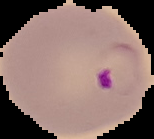

image size = 154×139 pixels
preparation = thin blood film
malaria status = parasitized
image type = segmented cell region with the area outside set to black